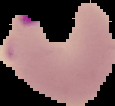
image type = segmented cell region on a black background
preparation = thin blood smear
malaria status = parasitized
image size = 115×106 pixels